Give the position of every Plasmodium parasite visible.
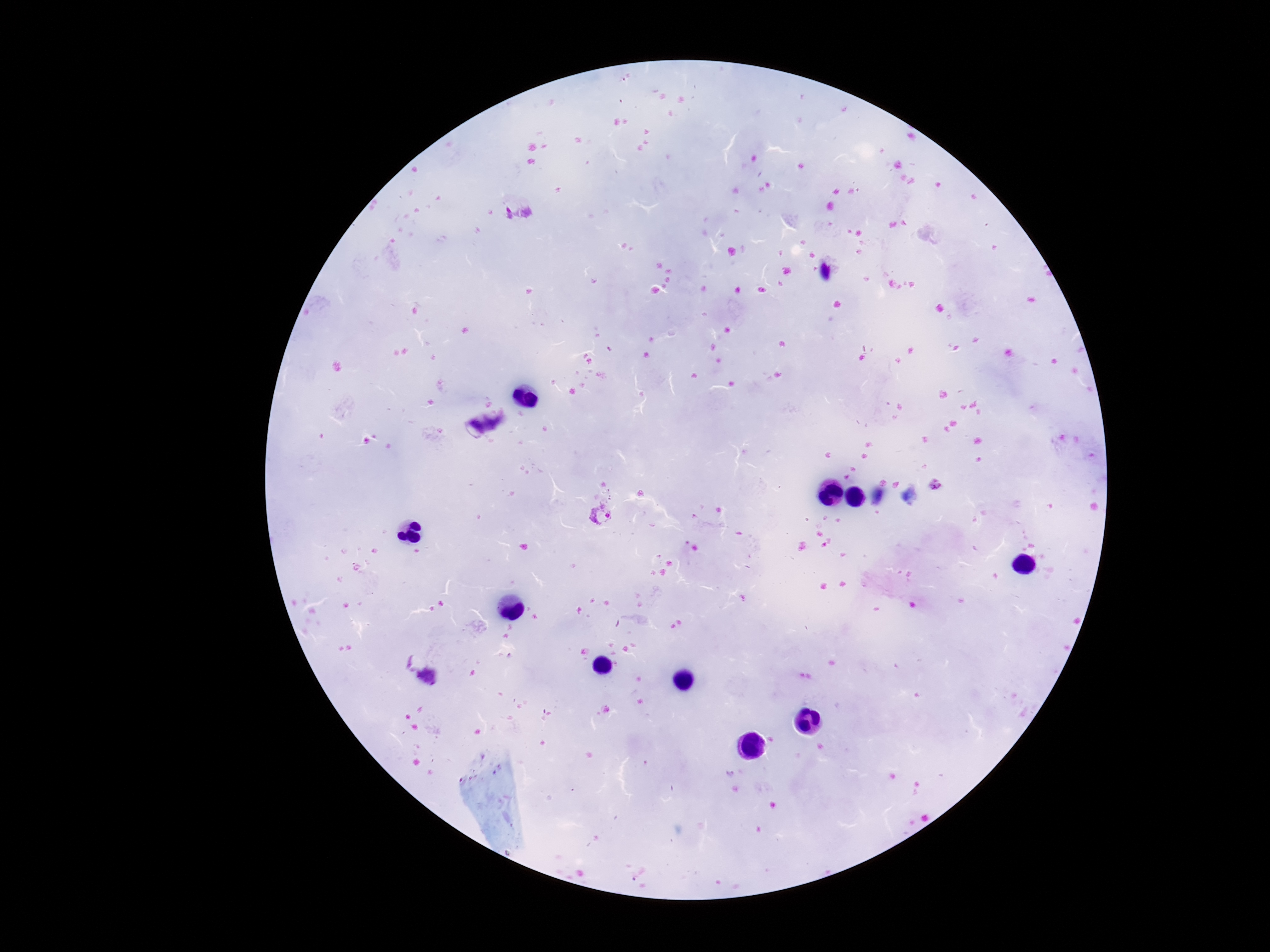
Approximate centers as [x, y] in pixels.
Plasmodium parasites: [514, 208], [936, 486], [600, 514].

Summary:
  - Stain: Giemsa
  - Magnification: 100x
  - Capture: smartphone camera through the microscope eyepiece
  - Field of view: one from this slide
  - Preparation: thick blood film
  - Patient malaria status: positive
  - Image size: 1270×952 pixels